Classify this cell by malaria status.
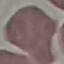

Uninfected.

Thin smear of blood. Giemsa stain. Photographed with a smartphone camera at the microscope eyepiece. Automatically extracted cell patch, resized to 64 × 64 pixels.